Name the cell type shown.
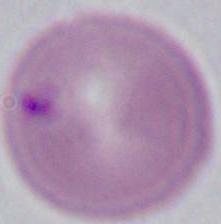
An erythrocyte.

Summary:
  - Magnification: 1000x
  - Modality: photomicrograph